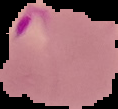
Summary:
  - Preparation: thin blood smear
  - Image type: segmented cell region on a black background
  - Malaria status: parasitized
  - Image size: 118×109 pixels